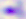

modality = photomicrograph
magnification = 400x
identification = Toxoplasma gondii